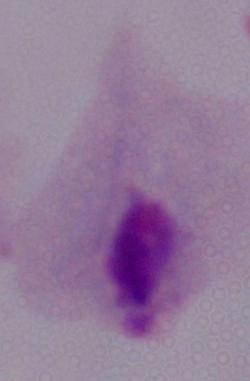
1000x magnification. A trichomonad is seen. Micrograph.